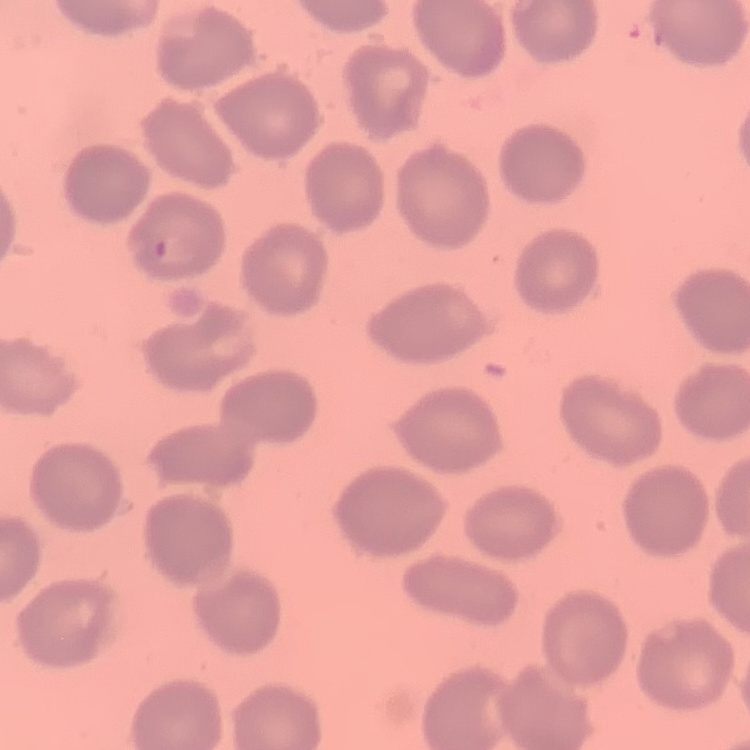
Summary:
  - Erythrocyte morphology: no rouleaux formation
  - Preparation: thin blood smear
  - Stain: Field's or Giemsa
  - Image type: square crop of a larger photomicrograph